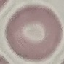

Result: negative for malaria parasites. Thin blood film. Cell patch, automatically extracted from a larger field of view and resized to 64 × 64 pixels. Acquired by smartphone through the microscope eyepiece. Giemsa-stained preparation.